State which parasite is depicted.
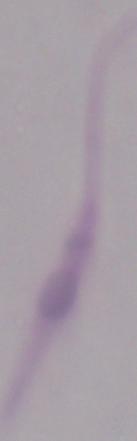

This is Leishmania.

Summary:
  - Modality: photomicrograph
  - Magnification: 1000x